Classify this cell by malaria status.
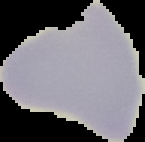
Uninfected.

Summary:
  - Image size: 145×142 pixels
  - Image type: cell region segmented out of the field of view; surrounding area masked to black
  - Preparation: thin blood smear